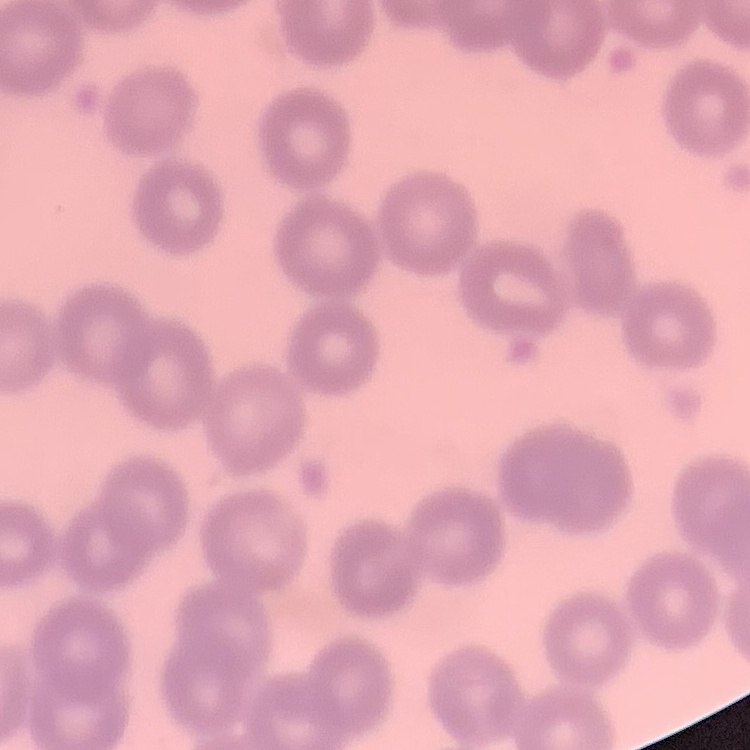
Summary:
  - Erythrocyte morphology: no rouleaux formation
  - Image type: square crop of a larger photomicrograph
  - Stain: Field's or Giemsa
  - Preparation: thin peripheral smear